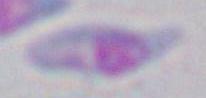
Summary:
  - Identification: Toxoplasma gondii
  - Magnification: 1000x
  - Modality: photomicrograph